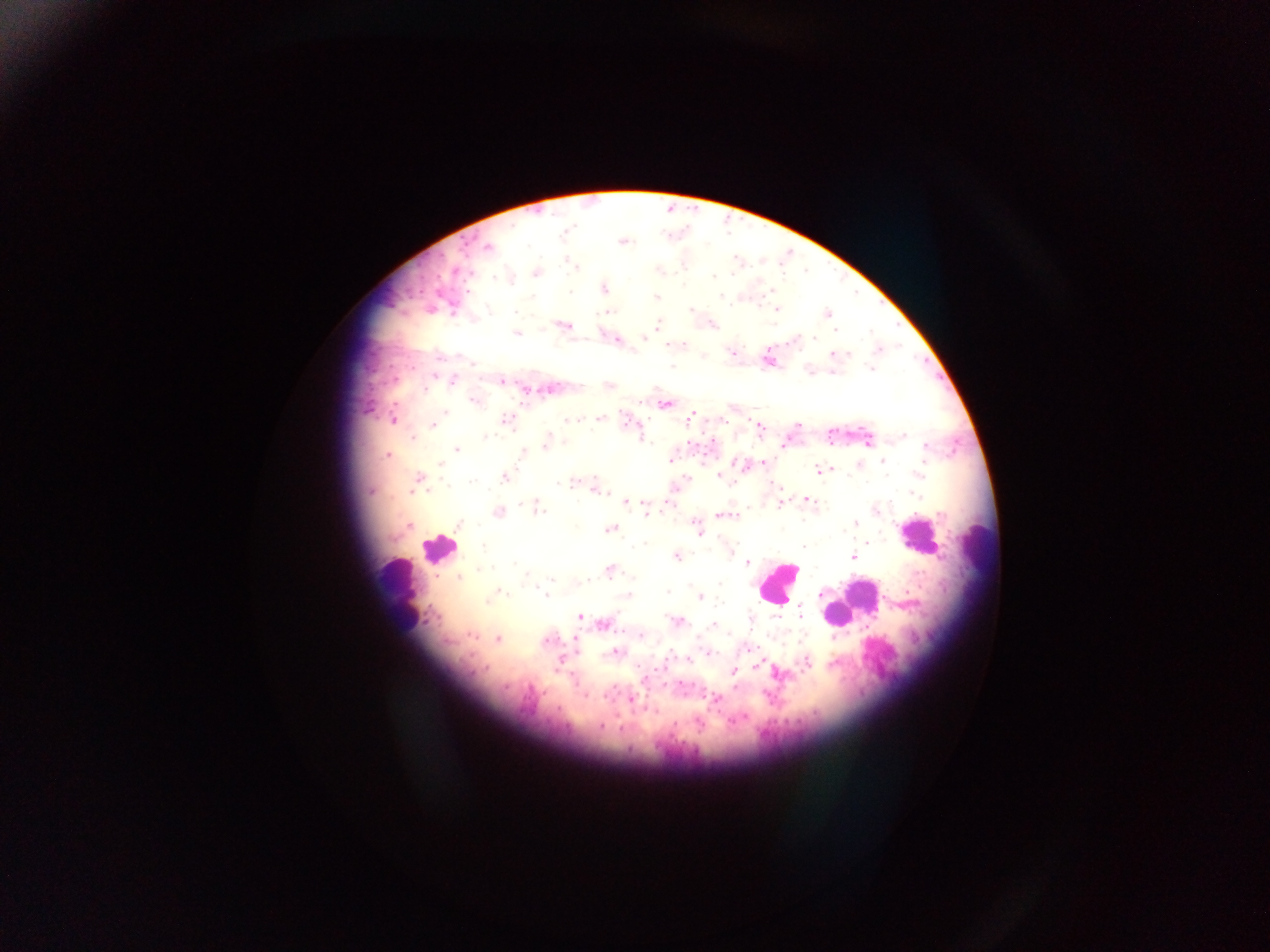
Approximate centers as x y in pixels. Leukocyte locations: 914 534; 982 546; 438 548; 777 582; 396 593; 865 596; 839 616. Malaria parasite locations: 564 232; 622 242; 488 247; 570 264; 576 267; 659 270; 455 271; 537 273; 732 275; 713 277; 511 280; 604 288; 772 291; 570 292; 721 295; 656 297; 776 309; 690 310; 515 311; 608 312; 827 314; 658 325; 565 326; 714 326; 835 330; 517 334; 649 336; 644 337; 814 338; 616 339; 684 345; 879 349; 731 352; 833 354; 846 355; 472 363; 671 366; 871 369; 832 372; 434 376; 453 381; 502 381; 425 391; 474 401; 666 405; 445 413; 691 416; 600 418; 392 419; 505 420; 689 420; 571 421; 722 421; 757 424; 797 425; 433 426; 488 433; 903 436; 413 437; 485 437; 643 439; 868 443; 546 444; 784 445; 927 447; 456 449; 387 454; 522 455; 670 461; 883 461; 736 462; 764 462; 440 464; 825 469; 819 470; 920 474; 719 476; 418 478; 505 478; 687 479; 571 482; 560 484; 731 484; 776 486; 598 491; 371 492; 915 494; 806 499; 626 502; 669 502; 522 503; 780 505; 536 507; 645 508; 875 509; 497 512; 646 514; 721 515; 695 523; 854 525; 409 526; 458 526; 610 529; 699 533; 867 542; 803 546; 482 547; 731 552; 677 557; 854 557; 748 563; 515 564; 483 570; 609 570; 459 577; 633 577; 553 579; 587 581; 719 585; 501 591; 668 592; 545 595; 626 595; 701 597; 488 601; 800 611; 580 617; 751 620; 680 622; 603 624; 713 625; 471 635; 642 635; 834 637; 575 639; 498 640; 545 641; 615 652; 710 653; 689 659; 560 661; 807 661; 755 667; 486 670; 733 670; 645 679; 506 688; 585 695; 717 699; 631 700; 654 712; 740 719; 732 721; 674 723; 600 727. Image is 1270×952 pixels. Thick blood smear. Mobile-phone photograph taken through the microscope. Collected in Ghana. Single field of view.